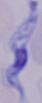

Photomicrograph. Captured at 1000x magnification. A trypanosome is shown.